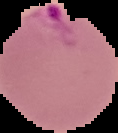 Image is 118×133 pixels. Malaria status: parasitized. From a thin blood smear. The area outside the segmented cell region is set to black.